Locate Plasmodium parasites and leukocytes.
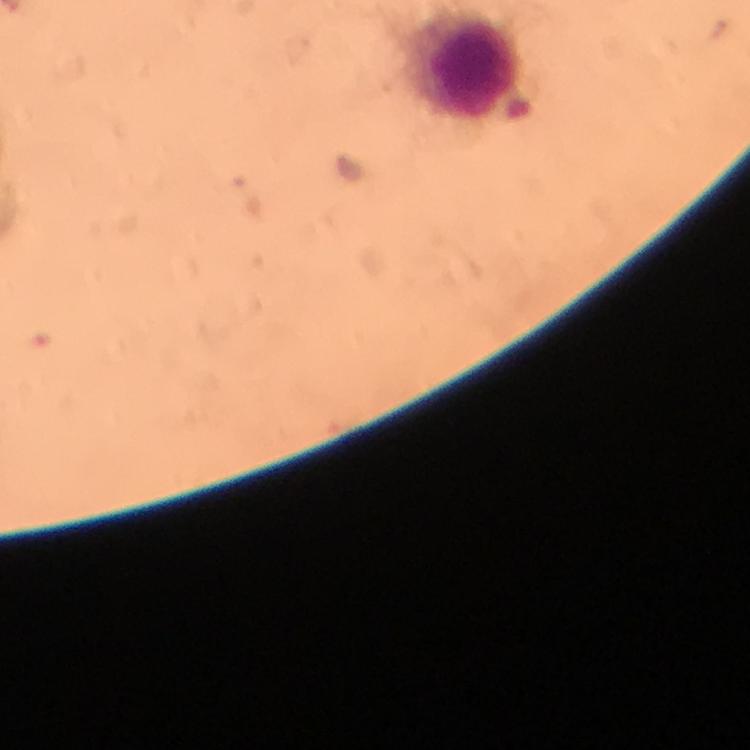
No Plasmodium parasites seen.
Approximate centers as [x, y] in pixels.
Leukocytes: [476, 67].

Cropped region of a single field of view. Giemsa stain. From a diagnostic examination for malaria. Photographed through the microscope with a smartphone camera. Image is 750×750 pixels. Immersion oil applied. Thick blood film. 100x magnification.